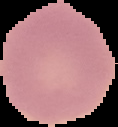
Summary:
  - Image size: 118×127 pixels
  - Preparation: thin blood film
  - Image type: segmented cell region with the area outside set to black
  - Malaria status: uninfected